Locate every blood parasite and identify its species.
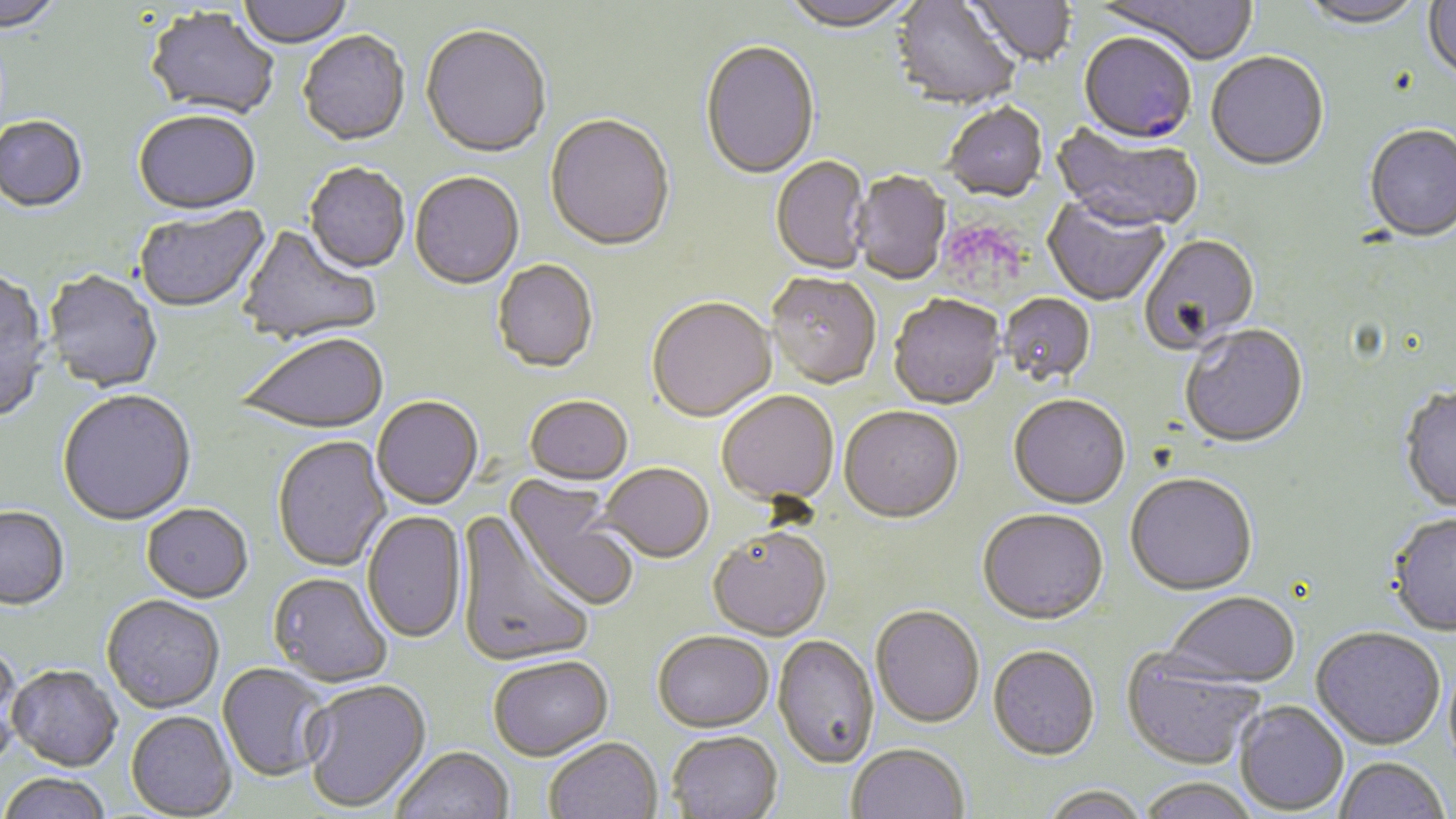
Approximate bounding boxes as (x1, y1, x2, y2) in pixels.
Plasmodium falciparum-infected red blood cells: (1078, 35, 1196, 147).
No Plasmodium ovale, Plasmodium malariae, Plasmodium vivax, Babesia divergens, or Trypanosoma brucei observed.

Uninfected red blood cell locations: (0, 0, 65, 36), (235, 0, 354, 50), (781, 0, 916, 35), (891, 0, 1019, 112), (966, 0, 1077, 69), (1098, 0, 1258, 67), (1299, 0, 1427, 31), (1423, 0, 1456, 84), (144, 9, 280, 122), (420, 27, 551, 161), (297, 33, 410, 149), (700, 43, 819, 181), (1206, 53, 1329, 174), (942, 105, 1048, 204), (133, 113, 261, 218), (545, 116, 675, 254), (0, 117, 89, 215), (1052, 123, 1203, 237), (1364, 126, 1456, 245), (771, 157, 871, 276), (304, 164, 410, 276), (852, 172, 950, 286), (409, 174, 525, 292), (1043, 198, 1169, 307), (134, 206, 271, 315), (238, 226, 382, 347), (1139, 235, 1260, 356), (492, 261, 599, 375), (0, 270, 51, 424), (42, 271, 163, 394), (765, 275, 881, 391), (999, 293, 1096, 388), (888, 297, 1006, 412), (646, 299, 777, 425), (1180, 326, 1308, 451), (236, 335, 390, 436), (1399, 387, 1456, 515), (57, 391, 197, 528), (716, 392, 840, 509), (524, 397, 633, 487), (1008, 397, 1130, 511), (372, 398, 483, 511), (839, 408, 964, 526), (272, 436, 392, 573), (600, 465, 714, 565), (1125, 475, 1258, 598), (504, 477, 639, 612), (141, 505, 253, 605), (0, 509, 70, 613), (457, 510, 594, 669), (977, 511, 1110, 628), (362, 512, 467, 645), (1387, 515, 1456, 638), (706, 529, 832, 643), (267, 573, 392, 689), (1163, 593, 1299, 693), (101, 597, 224, 715), (870, 607, 984, 730), (1310, 629, 1446, 753), (653, 634, 774, 736), (772, 637, 879, 771), (0, 645, 27, 769), (987, 647, 1100, 764), (1120, 652, 1263, 773), (489, 658, 613, 764), (216, 664, 332, 783), (8, 667, 123, 774), (302, 680, 432, 815), (1234, 702, 1349, 816), (126, 712, 237, 818), (667, 733, 783, 819), (545, 740, 662, 819), (847, 745, 970, 819), (391, 748, 514, 819), (1334, 759, 1449, 818), (0, 775, 112, 819), (1138, 780, 1259, 819), (1041, 788, 1149, 819). Slide-level diagnosis: Plasmodium falciparum. Image is 1456×819 pixels. Optical microscopy. May-Grünwald-Giemsa-stained preparation. 1000x magnification. One field of a larger specimen. Thin blood smear.